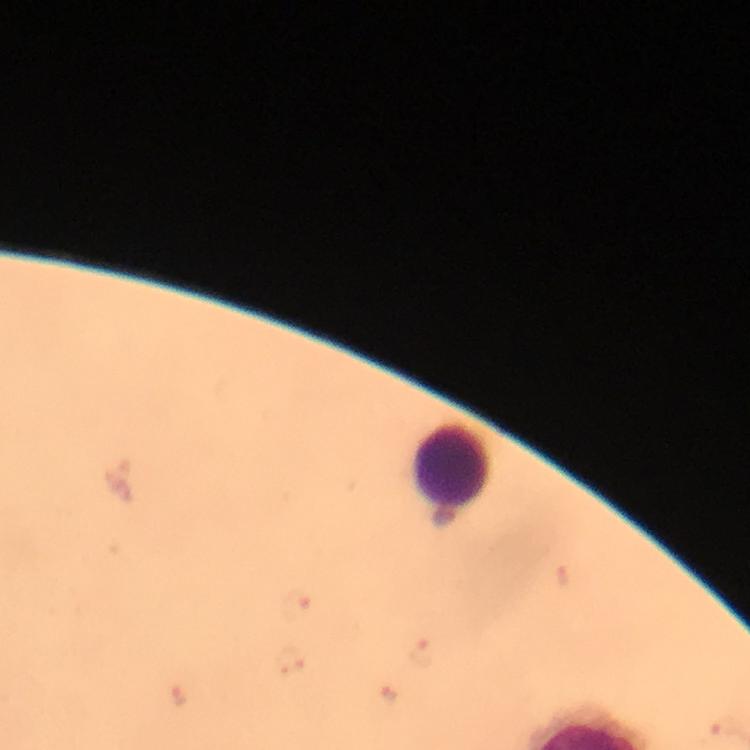

Approximate object centers, in pixels from the top-left corner.
Summary:
  - Leukocyte locations: (x=453, y=465)
  - Malaria parasite locations: (x=296, y=607), (x=423, y=654), (x=389, y=693), (x=179, y=696), (x=723, y=726)
  - Image size: 750×750 pixels
  - Magnification: 100x
  - Cropped from: a single field of view
  - Preparation: thick blood smear
  - Stain: Giemsa
  - Capture: smartphone mounted on the microscope
  - Context: from a diagnostic examination for malaria
  - Immersion oil: used